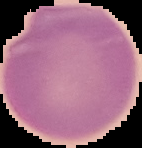

Summary:
  - Malaria status: uninfected
  - Image type: segmented cell region on a black background
  - Preparation: thin blood smear
  - Image size: 142×148 pixels